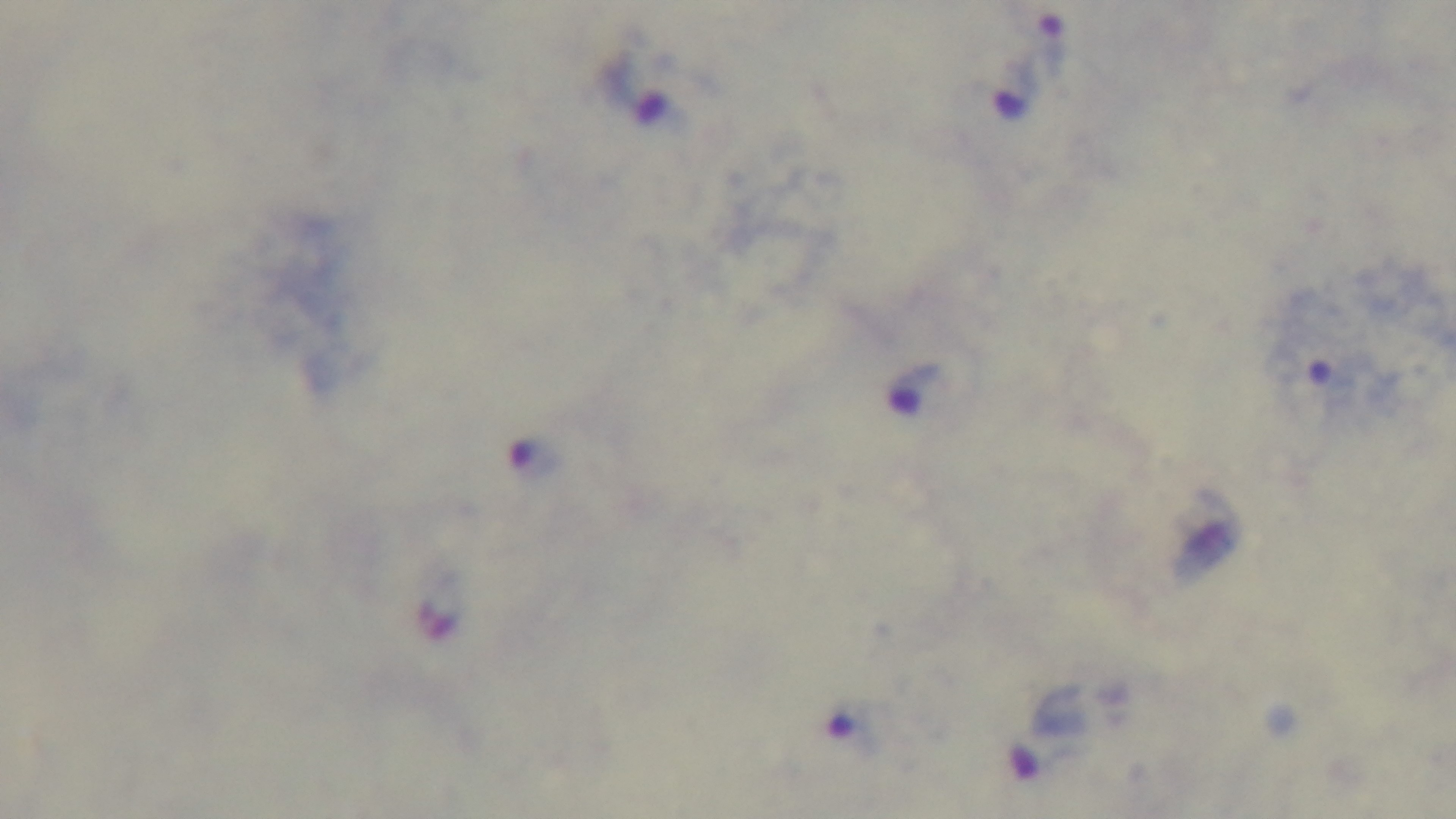
{
  "objective": "100x oil immersion",
  "preparation": "thick blood film",
  "modality": "light microscopy",
  "stain": "Giemsa",
  "malaria_status": "positive",
  "field_of_view": "one from the slide",
  "capture": "mounted 4K digital camera"
}